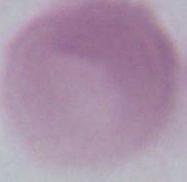
identification = red blood cell
modality = photomicrograph
magnification = 1000x